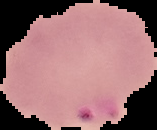
image size = 157×130 pixels
preparation = thin blood film
malaria status = parasitized
image type = segmented cell region on a black background